Locate every leukocyte (white blood cell).
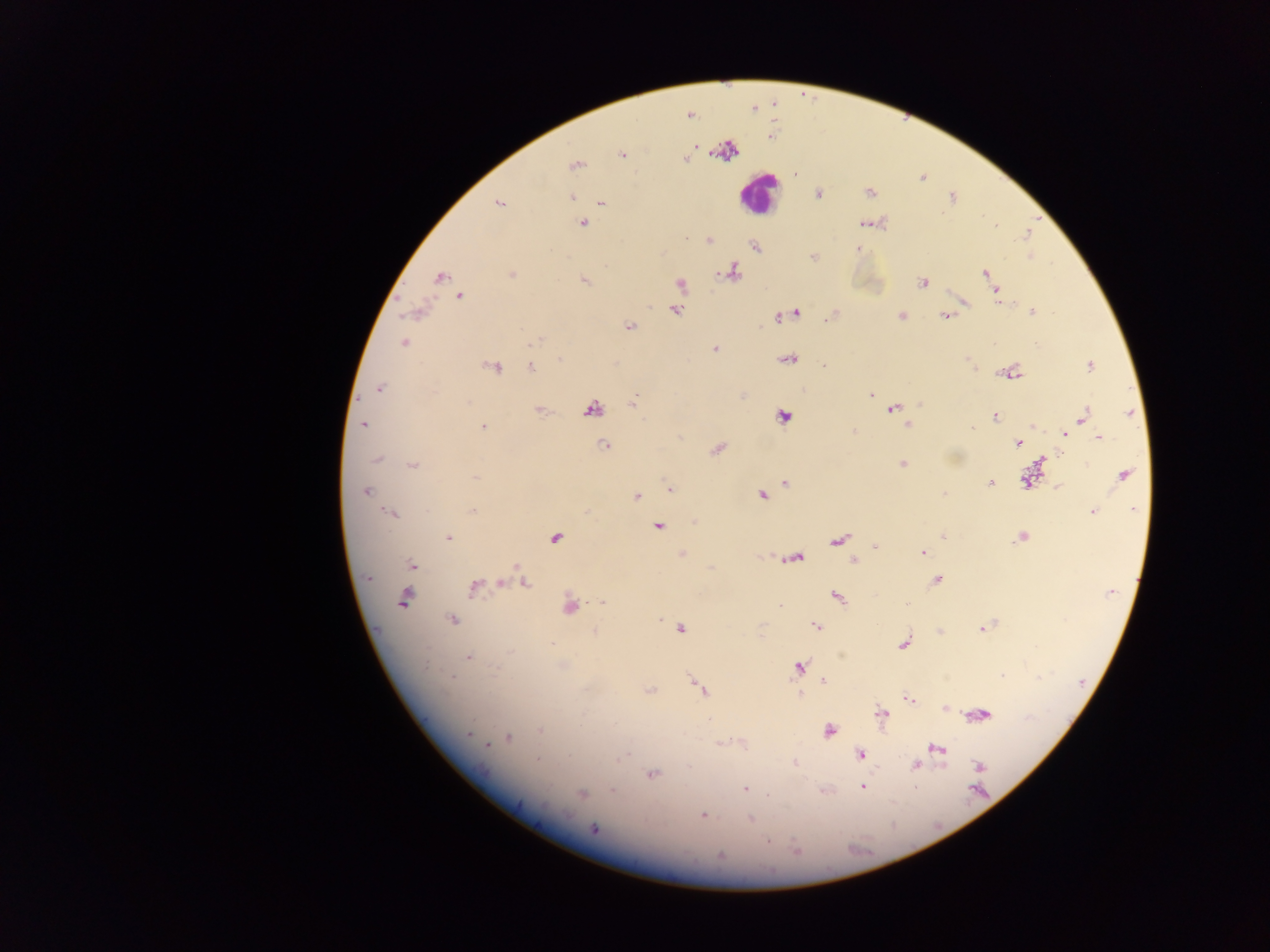
Approximate centers as x y in pixels.
Leukocytes: 758 193.

Malaria parasite locations: 690 116; 621 155; 685 160; 575 166; 869 192; 818 193; 572 197; 952 197; 601 203; 498 204; 584 224; 864 224; 1026 235; 686 239; 710 240; 755 246; 858 249; 813 256; 732 272; 985 272; 512 274; 441 277; 989 278; 584 280; 923 282; 680 284; 997 292; 459 296; 999 300; 965 302; 676 310; 1032 311; 796 313; 900 316; 829 317; 945 317; 778 318; 630 326; 536 341; 404 342; 714 349; 559 359; 788 359; 967 360; 824 366; 1090 366; 492 367; 530 368; 1013 372; 379 389; 870 395; 632 403; 919 405; 592 409; 893 410; 539 412; 1130 413; 1085 415; 995 416; 782 418; 363 424; 907 425; 482 427; 972 429; 1065 434; 1098 437; 1018 443; 604 446; 716 450; 1060 454; 377 460; 902 464; 413 465; 1124 474; 476 477; 1027 480; 990 482; 786 483; 1058 487; 669 489; 365 492; 944 493; 762 495; 637 497; 1134 508; 473 510; 1093 511; 586 512; 391 513; 694 522; 657 527; 944 536; 447 537; 555 538; 1020 538; 838 539; 876 547; 922 553; 681 554; 795 558; 853 561; 412 564; 517 565; 368 578; 936 580; 500 583; 526 584; 474 588; 1111 593; 837 597; 403 599; 603 603; 907 603; 780 605; 570 606; 659 619; 453 620; 816 626; 982 627; 679 629; 594 632; 551 643; 903 645; 510 652; 468 656; 426 665; 562 666; 798 668; 1002 675; 452 677; 824 681; 699 687; 650 690; 800 695; 909 699; 945 709; 881 714; 981 715; 540 730; 828 731; 469 734; 509 737; 488 744; 721 744; 938 748; 860 754; 623 756; 537 759; 794 763; 915 766; 980 766; 653 774; 914 786; 862 787; 745 788; 612 790; 581 794; 703 815; 751 818; 594 828; 768 842; 797 849; 720 856. One field of view. Thick blood smear. Sample from Ghana. Image is 1270×952 pixels. Photographed through a microscope with a mobile-phone camera.